Outline each uninfected red blood cell.
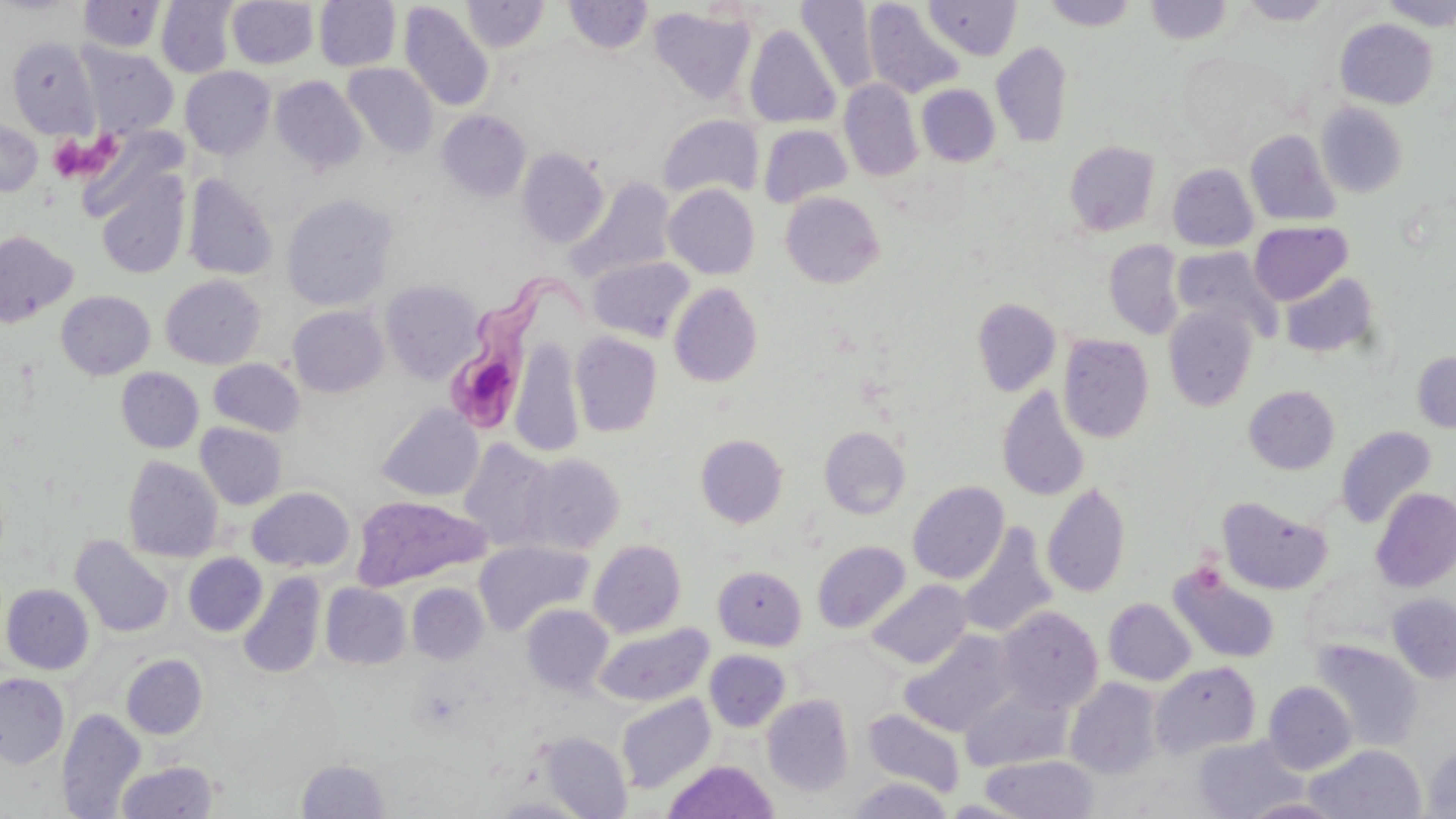
Approximate bounding boxes as (x1,y1)-(x2,y2) corner pairs in pixels.
Uninfected red blood cells: (314,0)-(401,71), (796,0)-(878,94), (1041,0)-(1140,30), (1379,0)-(1456,30), (78,1)-(165,53), (156,1)-(237,78), (226,1)-(318,69), (461,1)-(550,53), (564,1)-(653,54), (924,1)-(1022,60), (1144,1)-(1235,44), (1238,1)-(1335,25), (398,2)-(494,112), (863,2)-(966,99), (648,7)-(757,104), (1335,18)-(1438,109), (744,25)-(841,128), (7,36)-(100,138), (991,42)-(1073,148), (78,44)-(178,138), (1177,51)-(1290,149), (343,63)-(439,158), (180,66)-(276,159), (271,76)-(366,174), (839,79)-(922,182), (917,84)-(1000,166), (1316,102)-(1409,198), (437,110)-(532,201), (658,113)-(764,200), (0,120)-(43,196), (758,124)-(853,208), (1245,129)-(1342,226), (1064,140)-(1161,236), (517,148)-(609,249), (1167,164)-(1258,251), (97,174)-(189,280), (183,174)-(278,281), (569,177)-(676,284), (664,184)-(760,279), (780,191)-(885,288), (282,193)-(398,311), (1249,221)-(1353,305), (0,230)-(78,327), (1104,240)-(1184,340), (1171,246)-(1280,340), (587,256)-(694,343), (1280,272)-(1380,358), (160,275)-(266,369), (380,280)-(484,383), (668,283)-(764,387), (56,291)-(155,380), (971,298)-(1061,395), (288,305)-(388,397), (1163,305)-(1259,412), (570,332)-(662,437), (1058,334)-(1155,443), (510,337)-(584,457), (1411,351)-(1456,433), (209,359)-(305,436), (116,367)-(204,453), (996,384)-(1092,501), (1243,385)-(1340,474), (376,403)-(483,502), (196,423)-(287,509), (1336,425)-(1437,528), (819,426)-(911,518), (695,434)-(788,527), (459,439)-(558,551), (521,453)-(624,554), (122,456)-(223,562), (907,481)-(1009,584), (1042,481)-(1131,598), (247,487)-(355,572), (1371,487)-(1456,592), (351,495)-(491,591), (1217,496)-(1332,595), (957,523)-(1059,638), (70,535)-(174,637), (473,540)-(594,635), (588,540)-(686,638), (812,541)-(910,633), (184,553)-(266,636), (713,565)-(807,650), (1169,566)-(1281,664), (239,572)-(326,679), (867,579)-(972,669), (320,583)-(411,669), (407,583)-(488,664), (1,584)-(94,674), (1387,593)-(1456,683), (1103,598)-(1196,685), (522,604)-(614,696), (997,606)-(1103,714), (594,623)-(714,706), (900,630)-(1018,736), (1311,639)-(1424,751), (704,650)-(790,732), (121,654)-(207,739), (1150,662)-(1261,758), (0,673)-(69,769), (1066,678)-(1164,778), (1263,681)-(1357,774), (960,686)-(1073,771), (616,694)-(715,794), (762,695)-(854,797), (57,709)-(145,819), (864,709)-(965,797), (539,732)-(632,819), (1192,735)-(1308,819), (1422,744)-(1456,818), (1304,745)-(1426,819), (980,755)-(1099,819), (296,759)-(390,818), (663,760)-(778,818), (116,761)-(218,819), (849,777)-(953,818), (487,797)-(593,818), (1241,797)-(1348,818).

Trypanosoma brucei locations: (452,265)-(607,428). Platelet locations: (92,133)-(125,175), (50,134)-(90,180). Slide-level diagnosis: Trypanosoma brucei. Single field of view. 1000x magnification. May-Grünwald-Giemsa stain. Thin blood film. Image is 1456×819 pixels. Optical microscopy.